Evaluate for malaria.
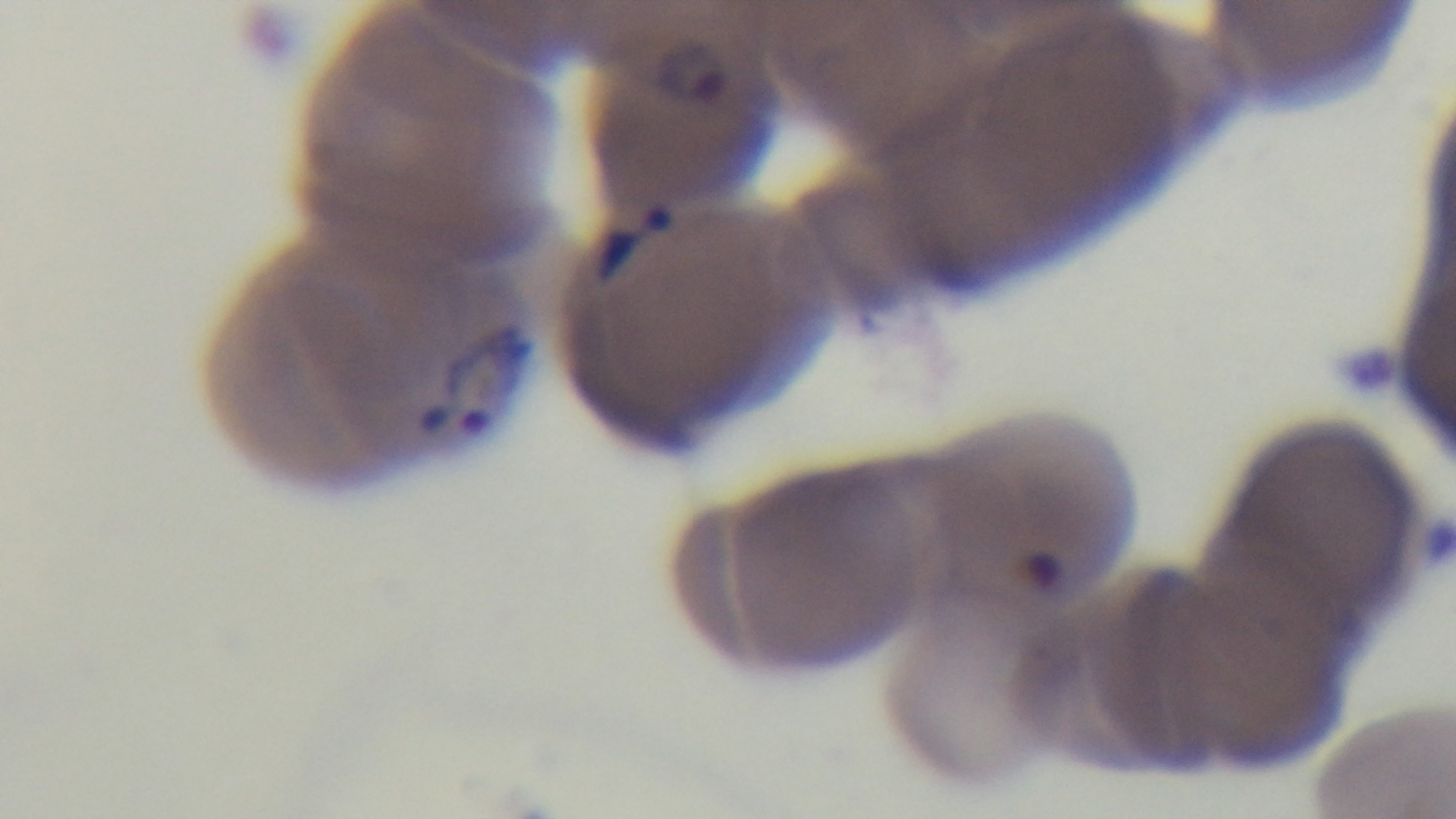

Infected.

Summary:
  - Modality: light microscopy
  - Stain: Giemsa
  - Preparation: thin smear
  - Objective: 100x oil immersion
  - Field of view: single
  - Capture: mounted 4K digital camera